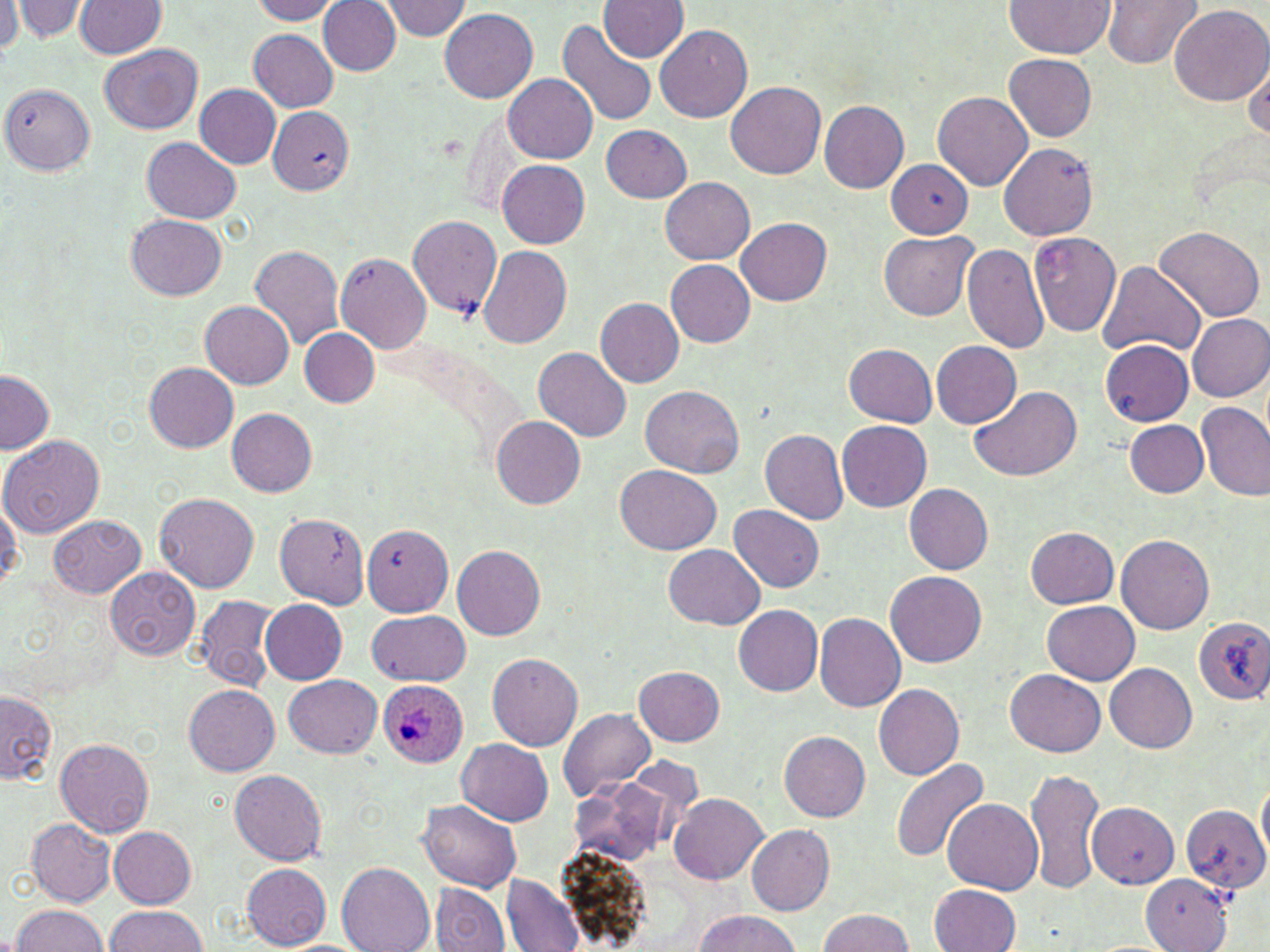

Summary:
  - Coordinate format: approximate bounding boxes as named x1/y1/x2/y2 corners in pixels
  - Uninfected red blood cell locations: (x1=251, y1=0, x2=344, y2=24), (x1=380, y1=0, x2=472, y2=40), (x1=600, y1=0, x2=689, y2=62), (x1=1103, y1=0, x2=1199, y2=68), (x1=1, y1=1, x2=21, y2=56), (x1=11, y1=1, x2=88, y2=40), (x1=75, y1=1, x2=166, y2=57), (x1=319, y1=1, x2=401, y2=74), (x1=1003, y1=1, x2=1114, y2=56), (x1=1167, y1=4, x2=1268, y2=107), (x1=438, y1=7, x2=538, y2=104), (x1=556, y1=19, x2=659, y2=127), (x1=655, y1=24, x2=752, y2=123), (x1=249, y1=30, x2=338, y2=111), (x1=101, y1=44, x2=203, y2=134), (x1=1244, y1=52, x2=1270, y2=148), (x1=1005, y1=54, x2=1097, y2=141), (x1=503, y1=73, x2=598, y2=163), (x1=727, y1=82, x2=825, y2=179), (x1=2, y1=84, x2=96, y2=173), (x1=196, y1=85, x2=281, y2=169), (x1=933, y1=91, x2=1033, y2=189), (x1=160, y1=97, x2=269, y2=211), (x1=818, y1=100, x2=909, y2=194), (x1=267, y1=107, x2=355, y2=195), (x1=601, y1=124, x2=691, y2=202), (x1=140, y1=138, x2=242, y2=223), (x1=998, y1=142, x2=1099, y2=240), (x1=498, y1=158, x2=591, y2=247), (x1=885, y1=162, x2=975, y2=238), (x1=660, y1=176, x2=755, y2=263), (x1=406, y1=214, x2=501, y2=316), (x1=126, y1=215, x2=225, y2=300), (x1=738, y1=218, x2=831, y2=304), (x1=1154, y1=225, x2=1265, y2=323), (x1=1027, y1=230, x2=1122, y2=338), (x1=880, y1=231, x2=977, y2=321), (x1=963, y1=242, x2=1050, y2=353), (x1=248, y1=244, x2=344, y2=347), (x1=477, y1=246, x2=574, y2=347), (x1=336, y1=253, x2=431, y2=353), (x1=666, y1=260, x2=755, y2=347), (x1=1094, y1=260, x2=1207, y2=360), (x1=596, y1=298, x2=684, y2=386), (x1=199, y1=301, x2=293, y2=389), (x1=1187, y1=312, x2=1270, y2=402), (x1=300, y1=329, x2=379, y2=408), (x1=1100, y1=339, x2=1195, y2=424), (x1=931, y1=340, x2=1021, y2=429), (x1=844, y1=344, x2=938, y2=427), (x1=534, y1=346, x2=630, y2=441), (x1=144, y1=361, x2=238, y2=452), (x1=0, y1=370, x2=53, y2=455), (x1=968, y1=384, x2=1082, y2=482), (x1=641, y1=386, x2=745, y2=478), (x1=1196, y1=402, x2=1270, y2=501), (x1=228, y1=408, x2=316, y2=497), (x1=492, y1=417, x2=585, y2=509), (x1=1124, y1=419, x2=1209, y2=497), (x1=837, y1=420, x2=931, y2=512), (x1=759, y1=427, x2=849, y2=525), (x1=0, y1=435, x2=105, y2=537), (x1=615, y1=465, x2=722, y2=555), (x1=904, y1=484, x2=993, y2=575), (x1=156, y1=494, x2=258, y2=592), (x1=0, y1=497, x2=21, y2=593), (x1=728, y1=505, x2=824, y2=592), (x1=272, y1=513, x2=371, y2=607), (x1=48, y1=514, x2=146, y2=598), (x1=362, y1=522, x2=453, y2=616), (x1=1025, y1=526, x2=1119, y2=609), (x1=1116, y1=532, x2=1214, y2=634), (x1=664, y1=544, x2=764, y2=629), (x1=453, y1=545, x2=545, y2=639), (x1=106, y1=566, x2=200, y2=660), (x1=886, y1=570, x2=986, y2=667), (x1=195, y1=594, x2=280, y2=692), (x1=259, y1=599, x2=348, y2=684), (x1=1042, y1=601, x2=1140, y2=684), (x1=734, y1=606, x2=822, y2=695), (x1=366, y1=610, x2=471, y2=686), (x1=814, y1=613, x2=907, y2=710), (x1=1194, y1=616, x2=1270, y2=704), (x1=487, y1=652, x2=583, y2=751), (x1=1106, y1=663, x2=1196, y2=751), (x1=634, y1=665, x2=725, y2=746), (x1=1005, y1=668, x2=1105, y2=756), (x1=284, y1=675, x2=381, y2=757), (x1=184, y1=684, x2=279, y2=775), (x1=874, y1=684, x2=964, y2=779), (x1=1, y1=688, x2=56, y2=785), (x1=560, y1=707, x2=654, y2=801), (x1=779, y1=731, x2=871, y2=820), (x1=55, y1=737, x2=154, y2=836), (x1=457, y1=738, x2=553, y2=826), (x1=890, y1=758, x2=989, y2=862), (x1=1026, y1=767, x2=1104, y2=895), (x1=230, y1=769, x2=327, y2=865), (x1=1257, y1=771, x2=1270, y2=863), (x1=571, y1=775, x2=670, y2=866), (x1=671, y1=792, x2=769, y2=884), (x1=942, y1=798, x2=1044, y2=894), (x1=419, y1=799, x2=522, y2=893), (x1=1087, y1=802, x2=1179, y2=887), (x1=1184, y1=805, x2=1268, y2=893), (x1=25, y1=819, x2=117, y2=907), (x1=746, y1=824, x2=835, y2=914), (x1=109, y1=827, x2=198, y2=907), (x1=338, y1=863, x2=435, y2=952), (x1=242, y1=864, x2=330, y2=949), (x1=1142, y1=873, x2=1231, y2=950), (x1=502, y1=874, x2=584, y2=951), (x1=431, y1=882, x2=512, y2=952), (x1=931, y1=884, x2=1021, y2=952), (x1=11, y1=905, x2=110, y2=952), (x1=105, y1=905, x2=208, y2=952), (x1=818, y1=908, x2=914, y2=952), (x1=692, y1=911, x2=800, y2=950)
  - Plasmodium ovale-infected red blood cell locations: (x1=377, y1=680, x2=468, y2=767)
  - Slide-level diagnosis: Plasmodium ovale
  - Preparation: thin blood film
  - Image size: 1270×952 pixels
  - Field of view: single
  - Stain: May-Grünwald-Giemsa
  - Magnification: 1000x
  - Modality: light microscopy